Point out each Plasmodium parasite.
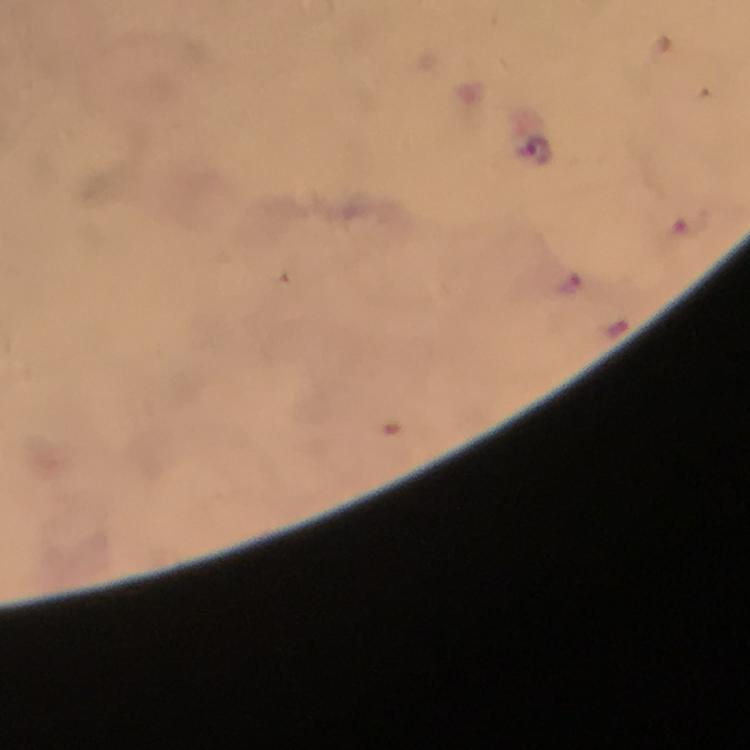
Approximate object centers, in pixels from the top-left corner.
Plasmodium parasites: (x=537, y=152), (x=691, y=221), (x=572, y=282).

preparation: thick blood film
cropped_from: a single field of view
image_size: 750×750 pixels
stain: Giemsa
capture: smartphone camera through the microscope
context: from a malaria diagnostic workup
immersion_oil: used
magnification: 100x